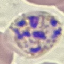
malaria status = parasitized
stain = Giemsa
preparation = thin smear
capture = smartphone through the microscope eyepiece
image type = automatically extracted cell patch, resized to 64 × 64 pixels